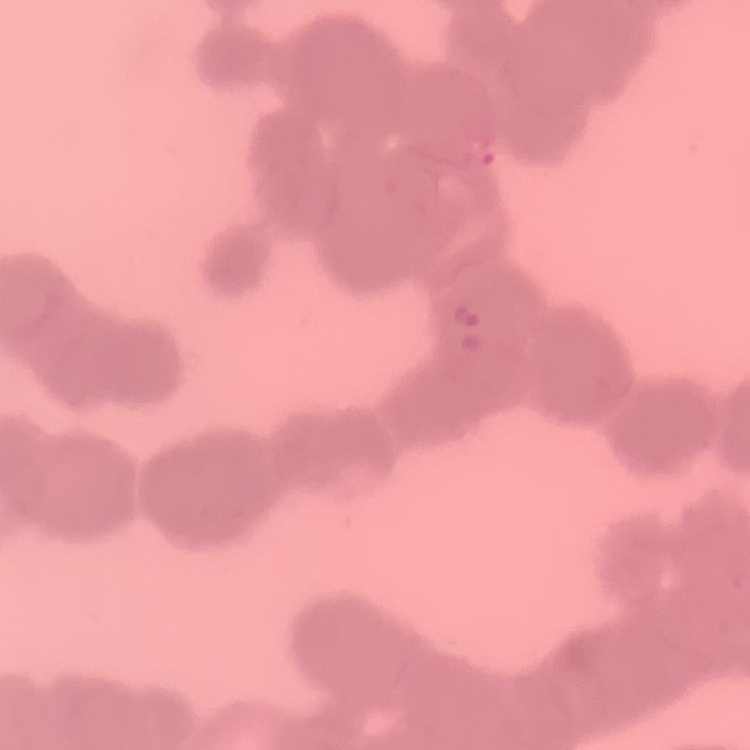

Summary:
  - Erythrocyte morphology: rouleaux formation
  - Image type: square crop of a larger photomicrograph
  - Stain: Field's or Giemsa
  - Preparation: thin blood smear